Point out every Plasmodium parasite and every leukocyte.
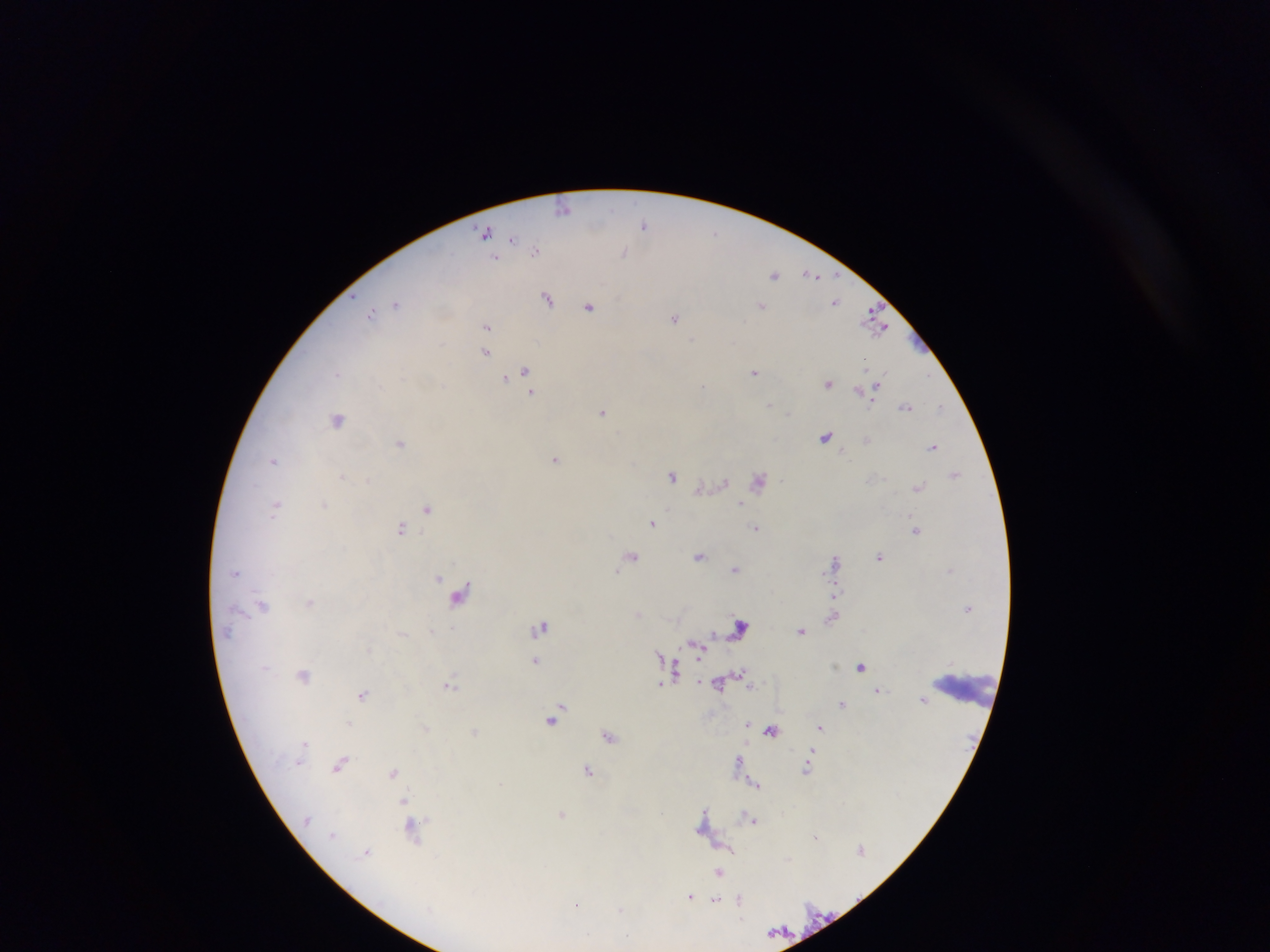
Approximate centers as (x, y) in pixels.
Plasmodium parasites: (615, 206), (562, 209), (645, 226), (716, 232), (485, 233), (513, 239), (535, 251), (622, 252), (495, 257), (811, 273), (774, 274), (547, 298), (837, 301), (760, 304), (397, 305), (589, 308), (371, 313), (871, 314), (676, 319), (693, 339), (866, 368), (526, 370), (336, 373), (754, 373), (504, 379), (880, 383), (703, 385), (828, 385), (858, 389), (533, 393), (770, 405), (906, 406), (942, 407), (602, 413), (401, 443), (933, 447), (553, 459), (274, 463), (955, 473), (673, 476), (342, 477), (367, 480), (725, 482), (759, 482), (919, 487), (324, 505), (278, 506), (742, 506), (427, 511), (653, 523), (401, 527), (756, 529), (916, 531), (631, 555), (700, 557), (879, 557), (836, 561), (735, 568), (439, 578), (465, 588), (837, 593), (310, 602), (262, 606), (432, 630), (535, 630), (802, 630), (402, 635), (695, 644), (660, 655), (536, 660), (862, 667), (678, 670), (305, 673), (743, 675), (661, 683), (451, 684), (749, 684), (362, 694), (924, 700), (843, 703), (553, 715), (351, 723), (749, 723), (821, 726), (425, 727), (475, 731), (772, 731), (609, 736), (304, 741), (739, 759), (340, 763), (300, 765), (589, 769), (392, 771), (757, 784), (403, 801), (705, 811), (561, 812), (756, 820), (700, 829), (412, 831), (331, 834), (814, 836), (729, 848), (366, 850), (720, 873), (690, 896), (715, 900), (740, 900), (576, 905), (621, 909), (774, 930).
No leukocytes observed.

Summary:
  - Capture: mobile-phone photograph through a microscope
  - Field of view: single
  - Country: Ghana
  - Image size: 1270×952 pixels
  - Preparation: thick blood smear